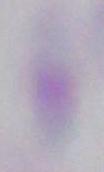

Summary:
  - Magnification: 1000x
  - Modality: micrograph
  - Identification: Toxoplasma gondii